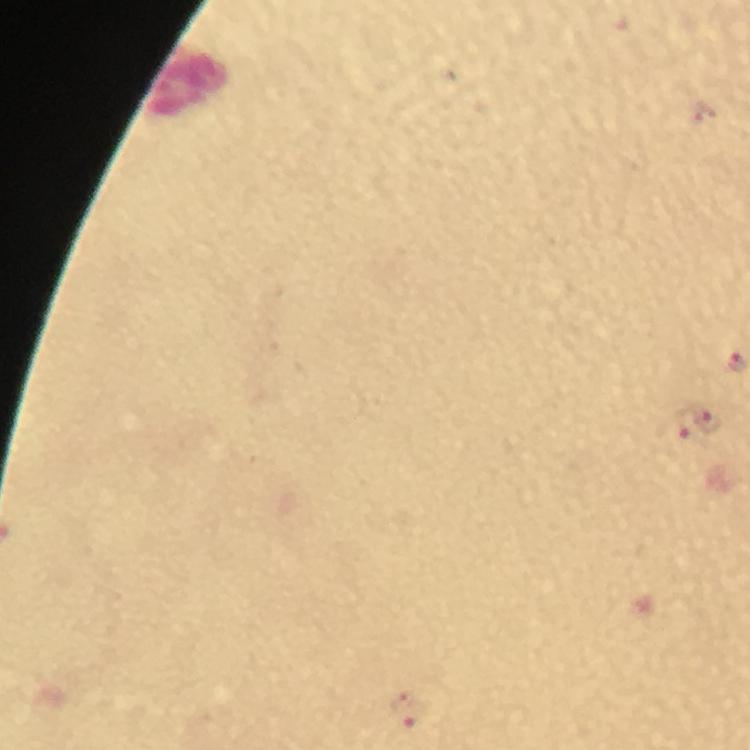
Approximate centers as (x, y) in pixels.
Summary:
  - Malaria parasite locations: (707, 420), (672, 431), (407, 708)
  - Context: from a diagnostic examination for malaria
  - Stain: Giemsa
  - Magnification: 100x
  - Preparation: thick blood smear
  - Capture: smartphone camera through the microscope
  - Immersion oil: used
  - Image size: 750×750 pixels
  - Cropped from: one field of view